Outline every artifact (platelet-like body, stain precipitate, or debris).
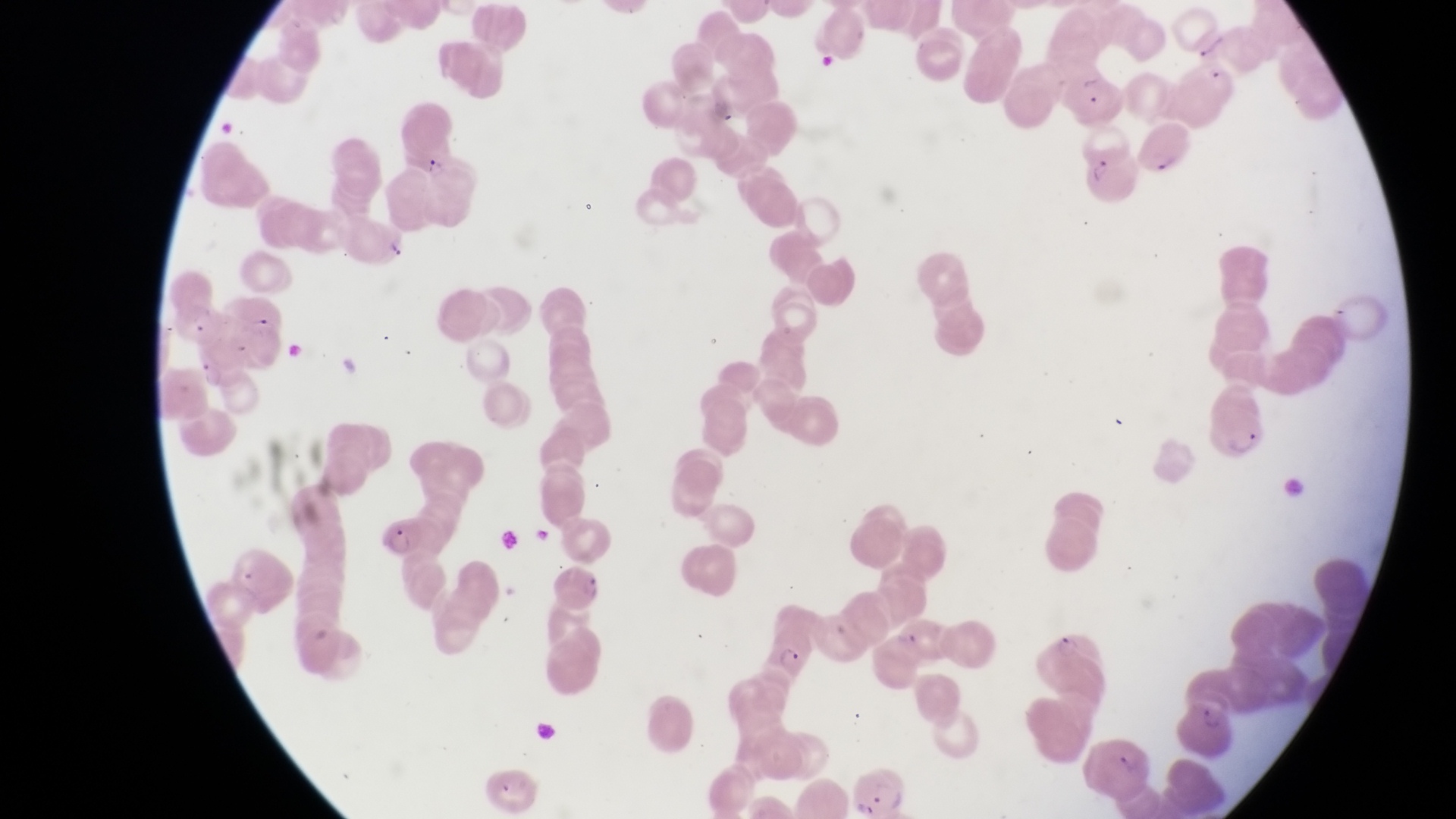

Approximate bounding boxes as (left, top, right, bottom) in pixels.
Artifacts (platelet-like body, stain precipitate, or debris): (388, 240, 414, 266).

Parasitised red blood cell locations: (1062, 66, 1126, 127), (1141, 125, 1193, 174), (1084, 148, 1137, 203), (175, 304, 227, 344), (373, 515, 432, 567), (761, 626, 810, 678), (1181, 706, 1231, 758), (1081, 735, 1153, 796), (849, 767, 909, 814). Trophozoite locations: (420, 158, 446, 184). Image is 1456×819 pixels. Collected in Uganda. Thin blood film. Photographed through the eyepiece of an Olympus CX-23 microscope with a smartphone camera. Magnification of 1000x. Single field of view.